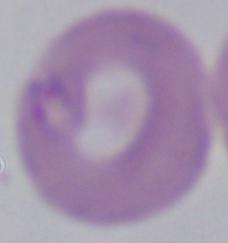
modality = photomicrograph
identification = Babesia
magnification = 1000x